Report the malaria status of this cell.
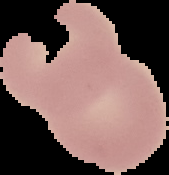
It is uninfected.

preparation = thin blood smear
image type = segmented cell region with the area outside set to black
image size = 169×175 pixels